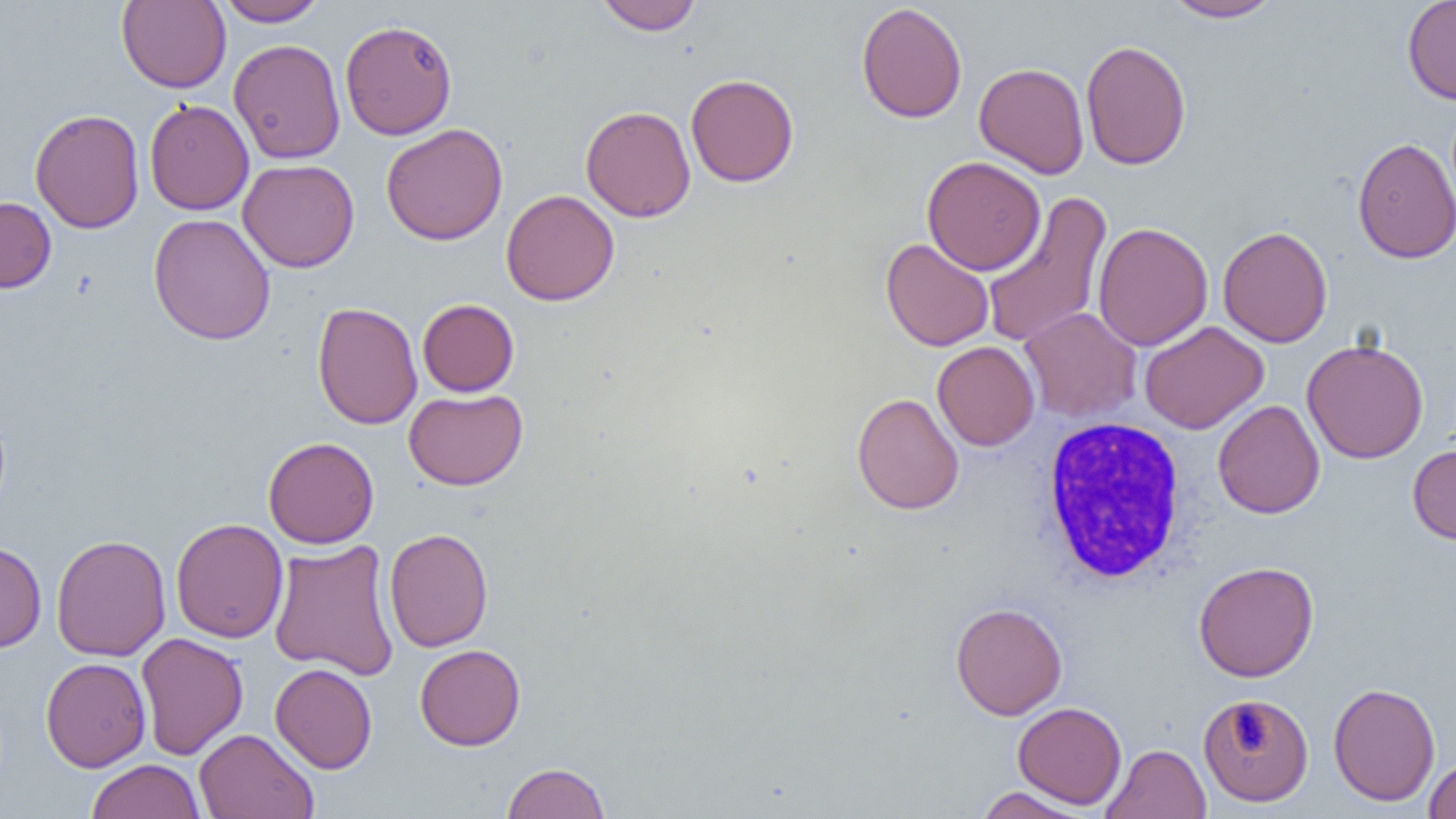 Approximate bounding boxes as named x1/y1/x2/y2 corners in pixels. Uninfected red blood cell locations: (x1=116, y1=0, x2=231, y2=93), (x1=216, y1=0, x2=327, y2=27), (x1=596, y1=0, x2=703, y2=35), (x1=1162, y1=0, x2=1286, y2=23), (x1=1402, y1=0, x2=1456, y2=105), (x1=856, y1=3, x2=967, y2=124), (x1=339, y1=20, x2=457, y2=141), (x1=228, y1=38, x2=346, y2=164), (x1=1080, y1=40, x2=1192, y2=170), (x1=974, y1=62, x2=1090, y2=179), (x1=686, y1=73, x2=799, y2=188), (x1=144, y1=99, x2=254, y2=215), (x1=581, y1=105, x2=696, y2=222), (x1=29, y1=109, x2=146, y2=234), (x1=380, y1=123, x2=508, y2=245), (x1=1352, y1=136, x2=1456, y2=264), (x1=922, y1=156, x2=1045, y2=276), (x1=237, y1=159, x2=360, y2=273), (x1=501, y1=189, x2=619, y2=306), (x1=980, y1=191, x2=1113, y2=349), (x1=0, y1=196, x2=56, y2=293), (x1=148, y1=213, x2=276, y2=345), (x1=1093, y1=222, x2=1213, y2=351), (x1=1218, y1=225, x2=1333, y2=348), (x1=880, y1=237, x2=995, y2=352), (x1=417, y1=299, x2=519, y2=396), (x1=312, y1=302, x2=422, y2=429), (x1=1020, y1=307, x2=1142, y2=422), (x1=1140, y1=321, x2=1268, y2=434), (x1=1301, y1=338, x2=1429, y2=464), (x1=932, y1=341, x2=1040, y2=451), (x1=404, y1=388, x2=528, y2=490), (x1=851, y1=392, x2=964, y2=515), (x1=1213, y1=400, x2=1325, y2=518), (x1=263, y1=436, x2=379, y2=549), (x1=1407, y1=444, x2=1456, y2=544), (x1=171, y1=518, x2=288, y2=643), (x1=384, y1=528, x2=494, y2=652), (x1=51, y1=534, x2=171, y2=662), (x1=267, y1=539, x2=401, y2=682), (x1=0, y1=541, x2=47, y2=653), (x1=1193, y1=561, x2=1319, y2=682), (x1=950, y1=602, x2=1067, y2=720), (x1=134, y1=632, x2=248, y2=760), (x1=414, y1=644, x2=526, y2=750), (x1=41, y1=657, x2=151, y2=772), (x1=270, y1=663, x2=377, y2=773), (x1=1328, y1=682, x2=1440, y2=806), (x1=1198, y1=692, x2=1314, y2=808), (x1=1013, y1=701, x2=1127, y2=809), (x1=194, y1=728, x2=319, y2=819), (x1=1102, y1=744, x2=1210, y2=819), (x1=1425, y1=757, x2=1456, y2=818), (x1=86, y1=759, x2=205, y2=819), (x1=501, y1=761, x2=610, y2=819), (x1=974, y1=786, x2=1092, y2=818). White blood cell locations: (x1=1039, y1=417, x2=1189, y2=585). Slide-level diagnosis: negative for blood parasites. Thin blood smear. Captured at 1000x magnification. Optical microscopy. Image is 1456×819 pixels. Single field of view.